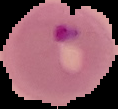

The area outside the segmented cell region is set to black. From a thin blood film. Result: Plasmodium parasites detected. Image is 118×109 pixels.